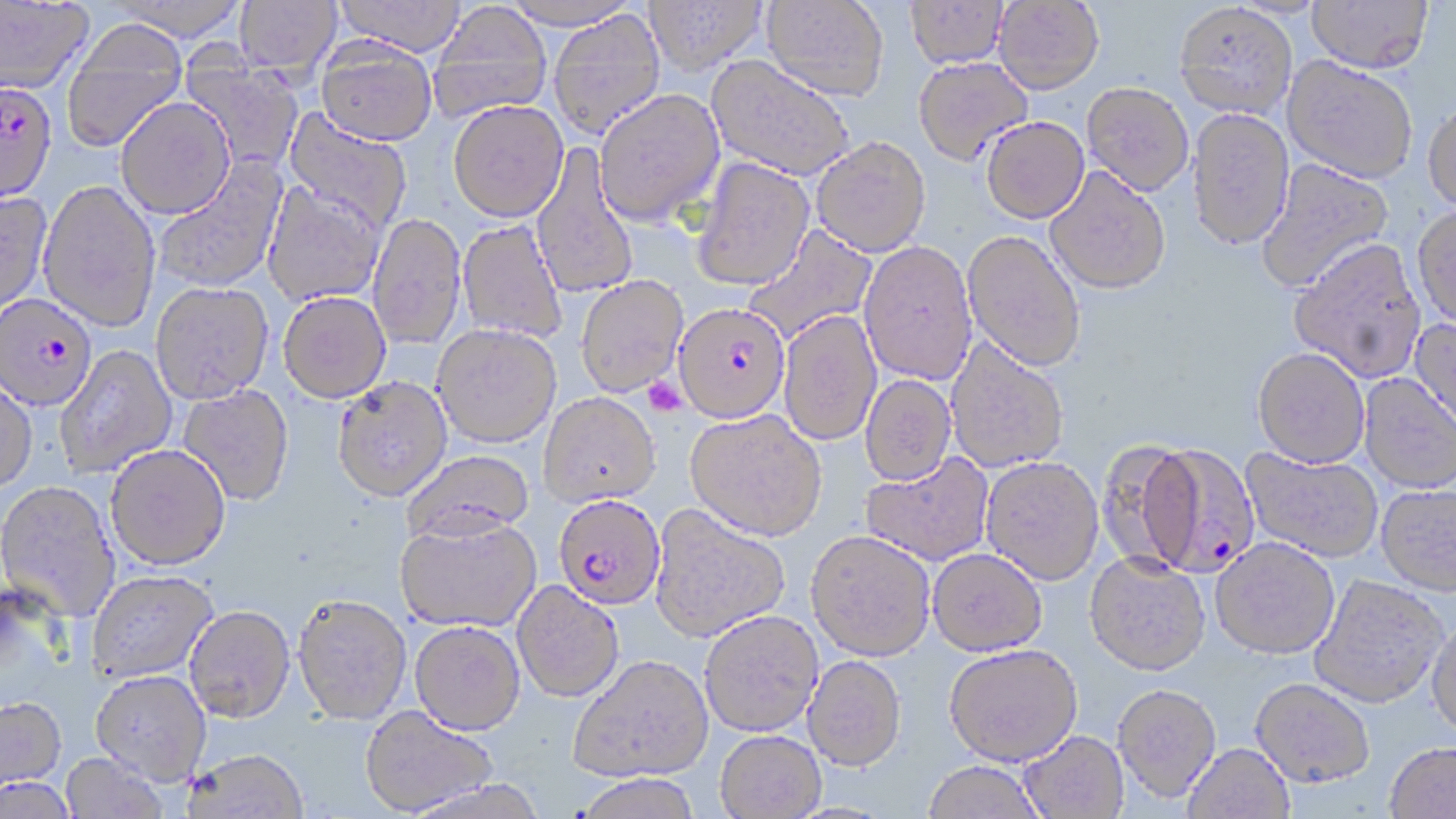
slide-level diagnosis = Plasmodium falciparum
platelet locations = approximate bounding boxes as named x1/y1/x2/y2 corners in pixels: (x1=643, y1=377, x2=688, y2=417)
magnification = 1000x
Plasmodium falciparum-infected red blood cell locations = approximate bounding boxes as named x1/y1/x2/y2 corners in pixels: (x1=0, y1=81, x2=57, y2=206), (x1=0, y1=293, x2=97, y2=411), (x1=675, y1=301, x2=790, y2=422), (x1=1142, y1=440, x2=1261, y2=577), (x1=553, y1=493, x2=666, y2=609)
stain = May-Grünwald-Giemsa
preparation = thin blood smear
modality = light microscopy
image size = 1456×819 pixels
field of view = one of a larger specimen
uninfected red blood cell locations = approximate bounding boxes as named x1/y1/x2/y2 corners in pixels: (x1=106, y1=0, x2=250, y2=41), (x1=334, y1=0, x2=468, y2=57), (x1=501, y1=0, x2=640, y2=30), (x1=644, y1=0, x2=766, y2=76), (x1=762, y1=0, x2=889, y2=100), (x1=905, y1=0, x2=1009, y2=68), (x1=994, y1=0, x2=1104, y2=93), (x1=1307, y1=0, x2=1434, y2=73), (x1=0, y1=1, x2=94, y2=95), (x1=234, y1=1, x2=342, y2=76), (x1=1174, y1=2, x2=1297, y2=119), (x1=428, y1=3, x2=552, y2=123), (x1=548, y1=10, x2=666, y2=140), (x1=61, y1=22, x2=189, y2=154), (x1=315, y1=38, x2=437, y2=146), (x1=177, y1=49, x2=305, y2=175), (x1=705, y1=56, x2=854, y2=181), (x1=1283, y1=56, x2=1419, y2=183), (x1=913, y1=57, x2=1033, y2=164), (x1=1083, y1=82, x2=1193, y2=195), (x1=593, y1=87, x2=725, y2=226), (x1=116, y1=98, x2=235, y2=218), (x1=448, y1=99, x2=569, y2=221), (x1=1422, y1=100, x2=1456, y2=214), (x1=284, y1=108, x2=412, y2=233), (x1=1187, y1=108, x2=1294, y2=250), (x1=981, y1=116, x2=1089, y2=223), (x1=812, y1=136, x2=931, y2=256), (x1=531, y1=143, x2=639, y2=299), (x1=153, y1=157, x2=288, y2=293), (x1=690, y1=157, x2=814, y2=290), (x1=1255, y1=159, x2=1394, y2=294), (x1=1045, y1=166, x2=1171, y2=294), (x1=38, y1=180, x2=161, y2=332), (x1=263, y1=181, x2=385, y2=306), (x1=0, y1=189, x2=52, y2=315), (x1=1412, y1=204, x2=1456, y2=329), (x1=367, y1=213, x2=466, y2=350), (x1=457, y1=219, x2=567, y2=344), (x1=743, y1=225, x2=877, y2=347), (x1=963, y1=229, x2=1087, y2=372), (x1=1288, y1=236, x2=1426, y2=382), (x1=858, y1=241, x2=977, y2=385), (x1=575, y1=275, x2=688, y2=397), (x1=150, y1=282, x2=273, y2=404), (x1=277, y1=291, x2=391, y2=403), (x1=779, y1=310, x2=882, y2=446), (x1=1412, y1=316, x2=1456, y2=438), (x1=431, y1=323, x2=561, y2=447), (x1=945, y1=338, x2=1069, y2=472), (x1=54, y1=345, x2=177, y2=477), (x1=1253, y1=347, x2=1369, y2=468), (x1=1360, y1=374, x2=1456, y2=493), (x1=860, y1=375, x2=957, y2=485), (x1=332, y1=376, x2=452, y2=502), (x1=0, y1=379, x2=37, y2=492), (x1=177, y1=385, x2=294, y2=506), (x1=539, y1=392, x2=660, y2=507), (x1=685, y1=409, x2=826, y2=540), (x1=1098, y1=435, x2=1201, y2=575), (x1=105, y1=444, x2=230, y2=569), (x1=1242, y1=448, x2=1383, y2=562), (x1=402, y1=449, x2=535, y2=542), (x1=861, y1=453, x2=994, y2=567), (x1=981, y1=457, x2=1104, y2=584), (x1=0, y1=480, x2=120, y2=622), (x1=1377, y1=483, x2=1456, y2=595), (x1=650, y1=504, x2=790, y2=641), (x1=395, y1=517, x2=541, y2=632), (x1=806, y1=530, x2=935, y2=661), (x1=1210, y1=537, x2=1339, y2=658), (x1=928, y1=548, x2=1047, y2=656), (x1=1084, y1=552, x2=1210, y2=675), (x1=85, y1=569, x2=218, y2=683), (x1=1310, y1=575, x2=1447, y2=708), (x1=512, y1=580, x2=624, y2=702), (x1=292, y1=594, x2=412, y2=724), (x1=184, y1=605, x2=295, y2=722), (x1=699, y1=609, x2=823, y2=737), (x1=1427, y1=616, x2=1456, y2=740), (x1=410, y1=620, x2=525, y2=735), (x1=944, y1=644, x2=1082, y2=766), (x1=568, y1=653, x2=714, y2=782), (x1=802, y1=655, x2=906, y2=771), (x1=90, y1=670, x2=211, y2=785), (x1=1250, y1=677, x2=1375, y2=787), (x1=1112, y1=682, x2=1221, y2=801), (x1=0, y1=697, x2=66, y2=793), (x1=359, y1=706, x2=498, y2=816), (x1=715, y1=730, x2=826, y2=818), (x1=1019, y1=730, x2=1128, y2=819), (x1=1384, y1=741, x2=1456, y2=818), (x1=1183, y1=742, x2=1294, y2=819), (x1=183, y1=748, x2=309, y2=819), (x1=61, y1=752, x2=168, y2=819), (x1=922, y1=760, x2=1046, y2=819), (x1=572, y1=774, x2=704, y2=819), (x1=0, y1=776, x2=77, y2=819)